State which cell type is depicted.
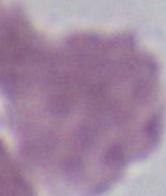
This is an erythrocyte.

Captured at 1000x magnification. Micrograph.